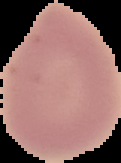 Result: no malaria parasites seen. From a thin blood film. Image is 121×163 pixels. Segmented cell region on a black background.